Give the position of every Plasmodium parasite visible.
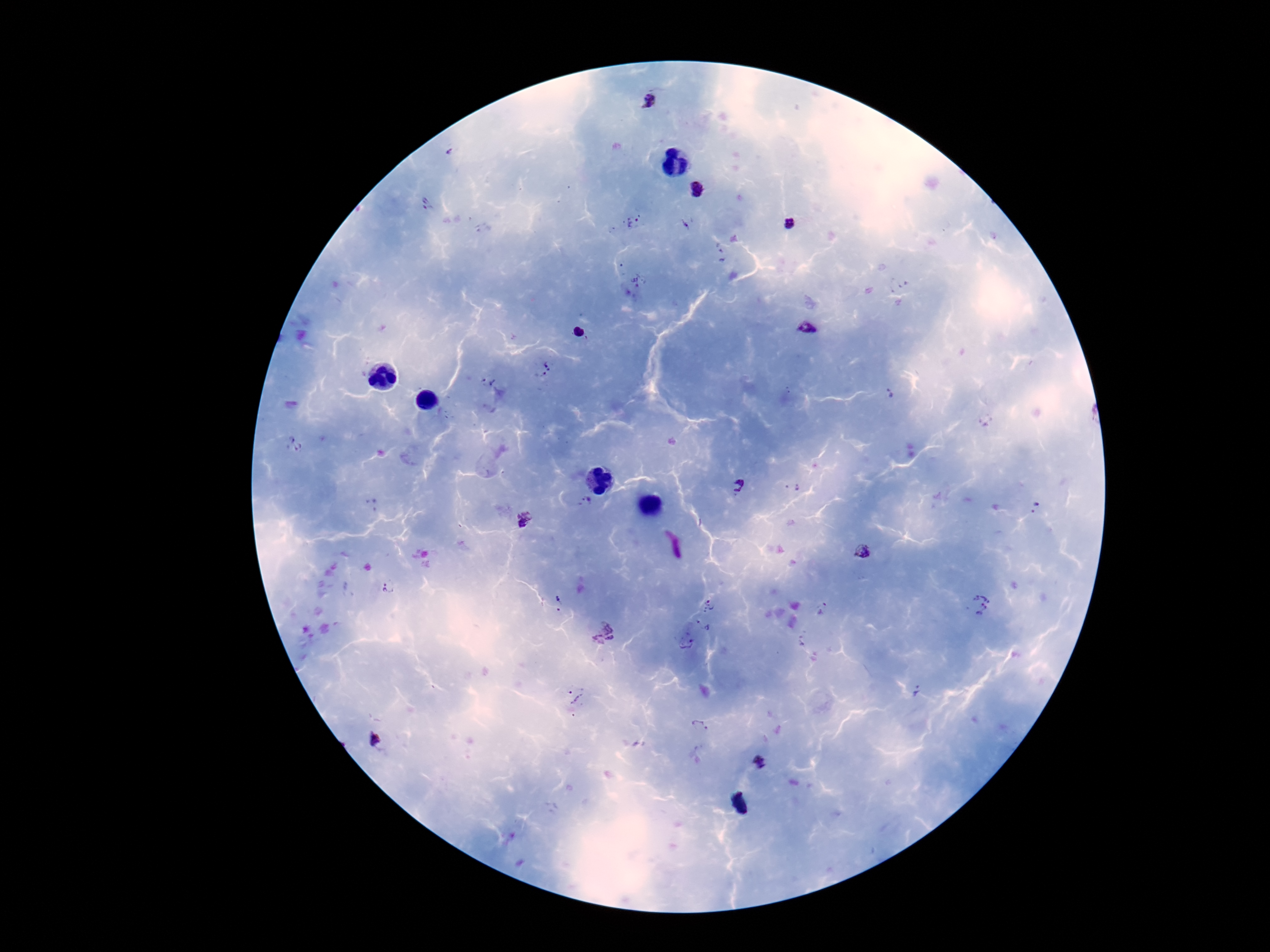
Approximate centers as [x, y] in pixels.
Plasmodium parasites: [651, 102], [695, 189], [427, 206], [632, 223], [789, 223], [687, 225], [636, 283], [807, 329], [580, 332], [549, 369], [487, 380], [293, 445], [737, 485], [586, 502], [525, 521], [863, 551], [387, 587], [557, 599], [709, 604], [977, 605], [823, 609], [702, 625], [602, 634], [685, 641], [918, 692], [573, 694], [700, 726], [375, 739], [762, 762].

capture = smartphone camera through the microscope eyepiece
preparation = thick blood film
magnification = 100x
field of view = one from this slide
image size = 1270×952 pixels
patient malaria status = positive
stain = Giemsa